State which parasite is depicted.
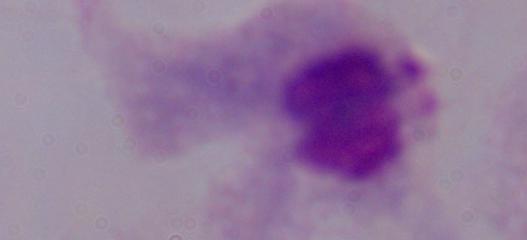
A trichomonad.

modality = micrograph
magnification = 1000x